Name the blood parasite species.
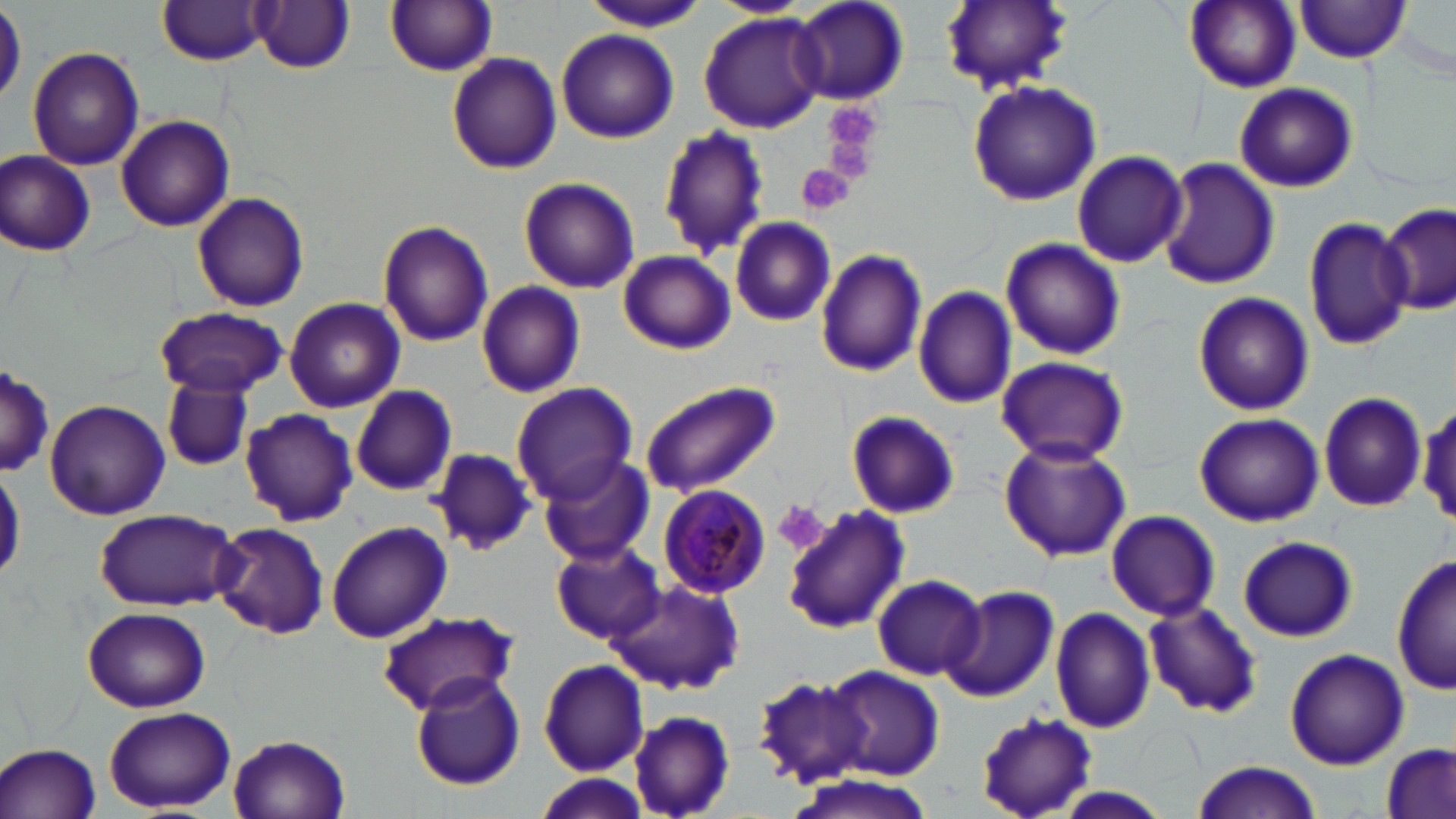
Plasmodium malariae.

modality = light microscopy
platelet locations = approximate bounding boxes as (x1, y1, x2, y2) in pixels: (824, 111, 883, 182), (798, 164, 857, 214), (772, 500, 829, 556)
image size = 1456×819 pixels
stain = May-Grünwald-Giemsa
magnification = 1000x
Plasmodium malariae-infected red blood cell locations = approximate bounding boxes as (x1, y1, x2, y2) in pixels: (657, 483, 771, 600)
uninfected red blood cell locations = approximate bounding boxes as (x1, y1, x2, y2) in pixels: (386, 0, 498, 75), (706, 0, 812, 16), (791, 0, 909, 107), (940, 0, 1072, 95), (1184, 0, 1300, 92), (1294, 0, 1414, 63), (156, 1, 275, 65), (251, 2, 356, 73), (584, 3, 707, 33), (0, 4, 24, 109), (698, 13, 824, 131), (556, 29, 678, 144), (27, 46, 144, 172), (446, 52, 562, 175), (967, 81, 1101, 207), (1234, 83, 1357, 193), (117, 114, 234, 231), (658, 126, 768, 260), (1, 149, 97, 257), (1071, 149, 1189, 268), (1158, 157, 1281, 289), (518, 176, 640, 292), (191, 192, 309, 312), (1376, 203, 1453, 313), (1302, 215, 1414, 351), (728, 216, 838, 326), (377, 221, 495, 347), (1001, 239, 1126, 359), (815, 248, 927, 377), (619, 250, 734, 355), (478, 281, 586, 399), (913, 286, 1019, 408), (1192, 292, 1315, 416), (285, 297, 405, 412), (152, 307, 288, 399), (994, 355, 1129, 464), (0, 361, 52, 482), (161, 379, 253, 473), (641, 381, 779, 497), (512, 382, 638, 505), (350, 385, 457, 497), (1318, 393, 1426, 512), (44, 399, 168, 519), (240, 408, 359, 528), (846, 411, 960, 519), (1193, 413, 1323, 527), (998, 436, 1131, 562), (428, 448, 537, 556), (536, 453, 652, 566), (0, 463, 24, 586), (782, 505, 908, 634), (93, 506, 243, 611), (1105, 509, 1221, 621), (326, 521, 451, 643), (208, 522, 328, 640), (1237, 536, 1356, 642), (551, 542, 664, 645), (1392, 554, 1455, 697), (872, 575, 985, 680), (611, 578, 743, 693), (943, 585, 1059, 702), (1142, 602, 1263, 719), (82, 606, 211, 712), (1051, 608, 1157, 734), (373, 610, 517, 716), (1283, 646, 1409, 769), (537, 659, 650, 775), (825, 665, 944, 779), (753, 674, 876, 788), (412, 676, 526, 791), (105, 707, 234, 812), (627, 711, 737, 817), (974, 711, 1099, 818), (229, 733, 352, 819), (1, 742, 102, 819), (1379, 745, 1453, 819), (1188, 761, 1323, 818), (534, 773, 653, 818), (788, 774, 935, 819)
field of view = single
preparation = thin blood film